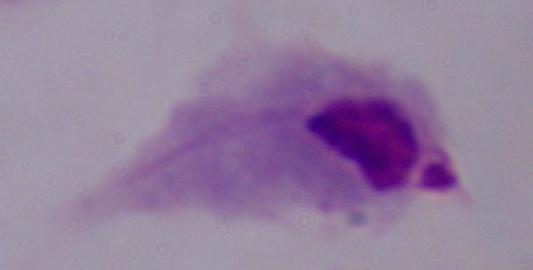

Summary:
  - Modality: micrograph
  - Identification: trichomonad
  - Magnification: 1000x